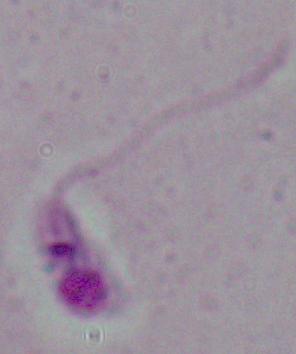

Photomicrograph. 1000x magnification. A Leishmania parasite is shown.